Give the extent of all Plasmodium falciparum-infected red blood cells.
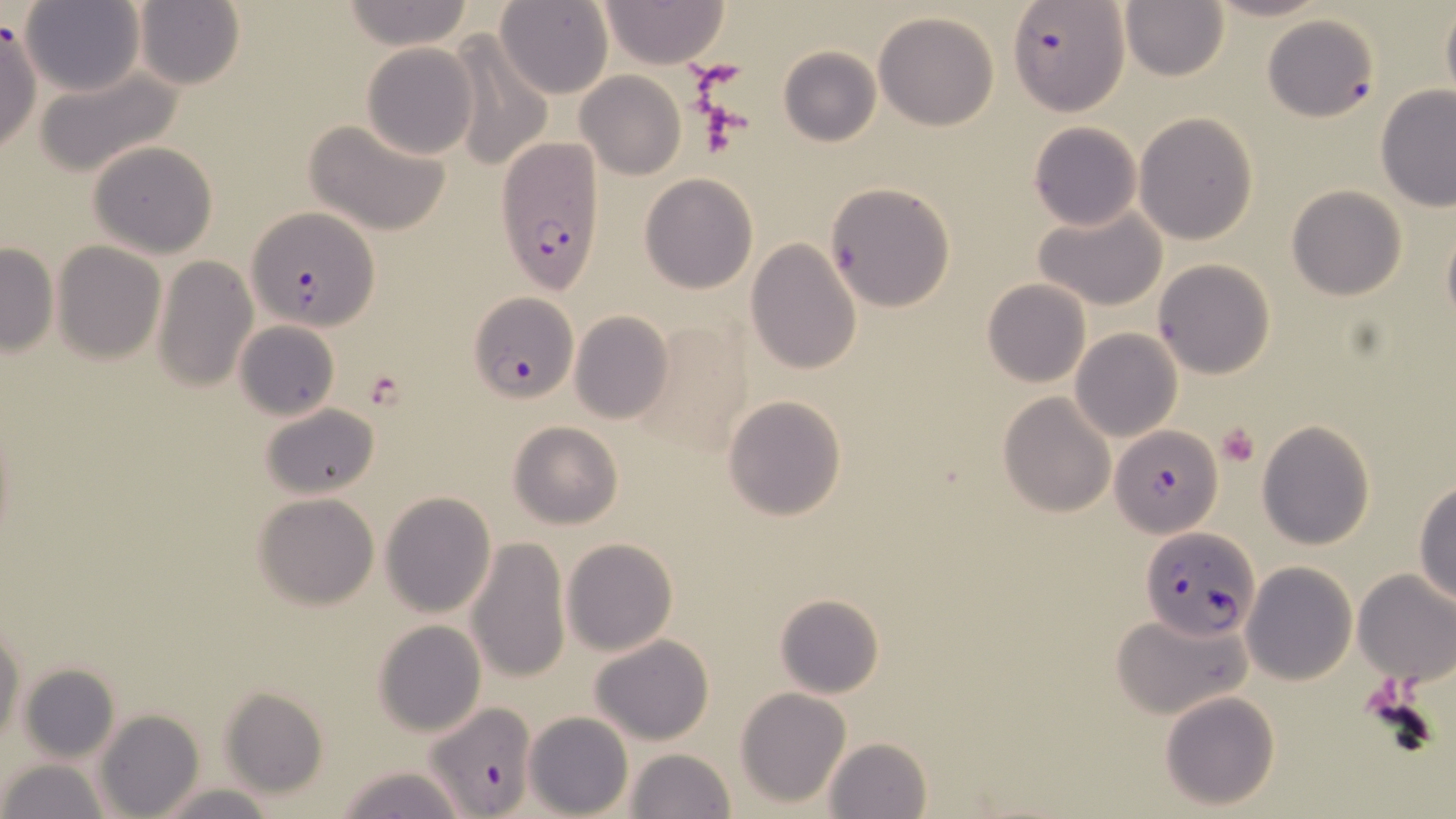
Approximate bounding boxes as (x1, y1, x2, y2) in pixels.
Plasmodium falciparum-infected red blood cells: (1009, 1, 1129, 114), (1263, 15, 1377, 123), (494, 136, 608, 296), (247, 207, 378, 332), (468, 293, 578, 401), (1112, 424, 1225, 538), (1138, 528, 1260, 646), (423, 706, 537, 819).

Summary:
  - Uninfected red blood cell locations: (341, 0, 475, 50), (600, 0, 728, 68), (1198, 0, 1335, 24), (134, 1, 246, 90), (496, 1, 613, 99), (1120, 1, 1231, 82), (20, 2, 145, 96), (1441, 2, 1456, 114), (873, 12, 999, 130), (0, 19, 43, 157), (446, 35, 554, 174), (361, 42, 479, 159), (778, 46, 880, 146), (37, 65, 185, 179), (577, 71, 684, 179), (1374, 84, 1456, 212), (1134, 112, 1258, 246), (305, 119, 452, 236), (1029, 121, 1143, 231), (87, 140, 219, 259), (640, 173, 757, 293), (825, 182, 955, 313), (1285, 185, 1407, 300), (1033, 204, 1169, 312), (1443, 219, 1456, 333), (747, 239, 862, 374), (50, 240, 167, 363), (0, 243, 58, 356), (153, 255, 258, 394), (1153, 258, 1275, 380), (982, 280, 1090, 388), (570, 312, 673, 424), (635, 315, 754, 456), (234, 320, 340, 421), (1070, 329, 1182, 443), (998, 392, 1116, 516), (723, 394, 848, 521), (258, 402, 380, 500), (1257, 419, 1376, 550), (508, 421, 625, 529), (1413, 478, 1456, 605), (254, 492, 380, 610), (381, 492, 497, 616), (466, 536, 571, 683), (562, 537, 678, 656), (1242, 562, 1358, 685), (1354, 568, 1456, 684), (774, 593, 885, 699), (1113, 613, 1250, 718), (373, 619, 488, 736), (0, 623, 24, 746), (589, 634, 714, 745), (17, 662, 121, 762), (220, 687, 329, 798), (736, 688, 851, 808), (1160, 690, 1281, 810), (95, 710, 204, 819), (524, 711, 633, 819), (823, 737, 933, 819), (624, 749, 737, 819), (2, 759, 107, 819), (334, 765, 470, 819), (154, 783, 279, 818)
  - Platelet locations: (694, 95, 751, 155), (1216, 423, 1260, 466)
  - Slide-level diagnosis: Plasmodium falciparum
  - Image size: 1456×819 pixels
  - Modality: light microscopy
  - Stain: May-Grünwald-Giemsa
  - Magnification: 1000x
  - Field of view: one of a larger specimen
  - Preparation: thin blood smear